Report the malaria status of this cell.
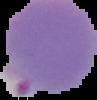
It is parasitized.

Summary:
  - Image type: cell region segmented out of the field of view; surrounding area masked to black
  - Preparation: thin blood film
  - Image size: 97×100 pixels